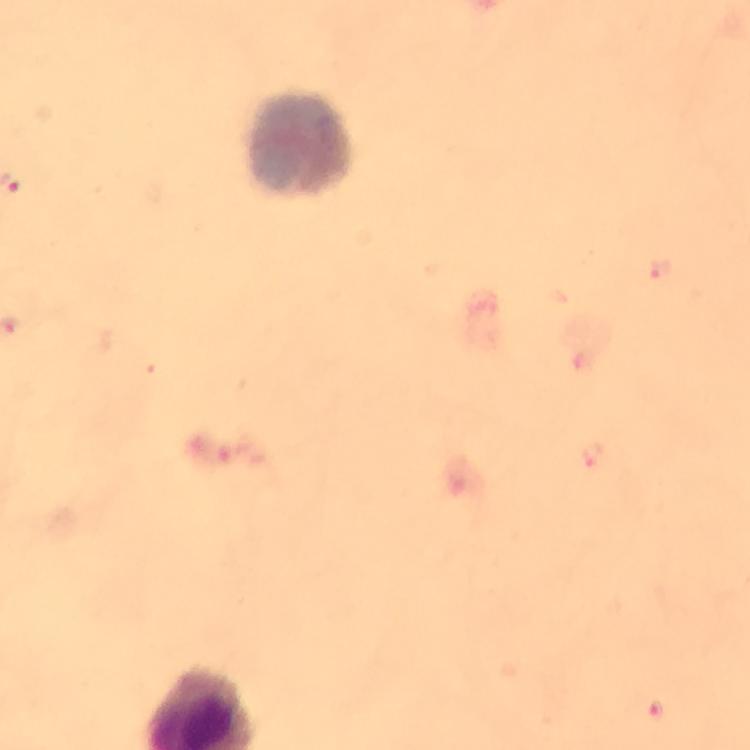

Approximate object centers, in pixels from the top-left corner. Leukocyte locations: (x=301, y=145). Malaria parasite locations: (x=661, y=269), (x=592, y=452), (x=657, y=708). From a malaria diagnostic workup. Photographed through the microscope with a smartphone camera. Immersion oil applied. Giemsa-stained preparation. Image is 750×750 pixels. Thick blood smear. Cropped region of a single field of view. At 100x magnification.